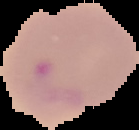
Summary:
  - Image size: 139×130 pixels
  - Result: malaria parasites detected
  - Preparation: thin blood smear
  - Image type: segmented cell region with the area outside set to black